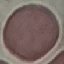 Malaria status: uninfected. Photographed with a smartphone camera at the microscope eyepiece. Cell patch, automatically extracted from a larger field of view and resized to 64 × 64 pixels. Thin blood smear. Giemsa-stained preparation.